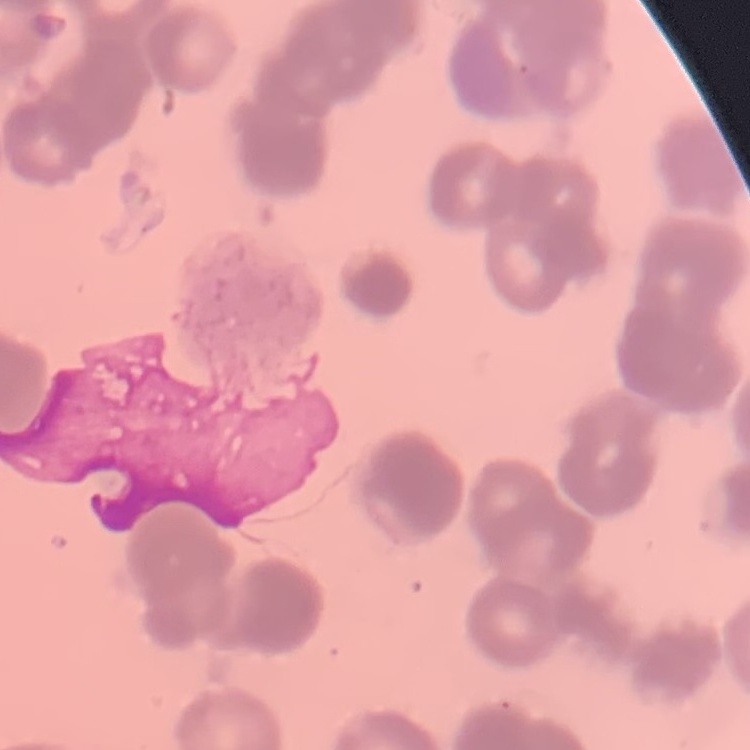
The red blood cells exhibit rouleaux formation. One tile cut from a larger photomicrograph. Thin blood smear. Field's or Giemsa stain.